Comment on the morphology of the erythrocytes.
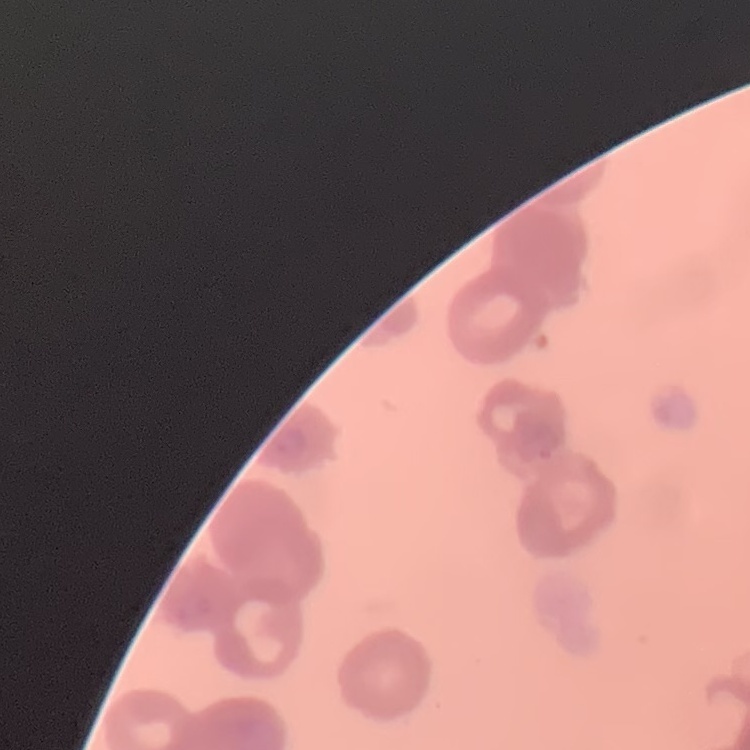

Rouleaux formation.

preparation = thin peripheral smear
stain = Field's or Giemsa
image type = one tile cut from a larger photomicrograph